Identify the preparation type.
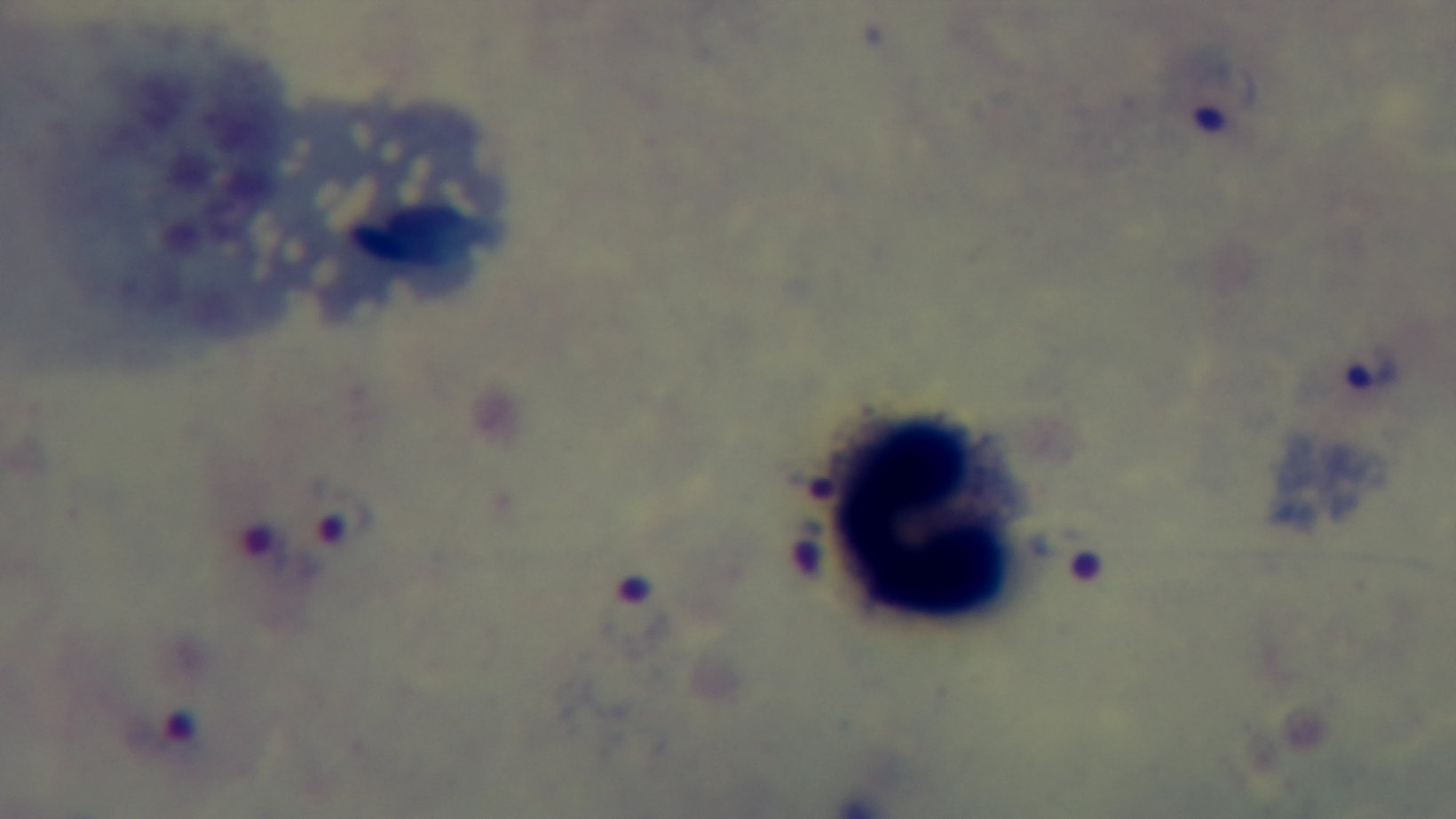
A thick smear.

Summary:
  - Field of view: single
  - Modality: light microscopy
  - Malaria status: infected
  - Objective: 100x oil immersion
  - Capture: mounted 4K digital camera
  - Stain: Giemsa